State which parasite is depicted.
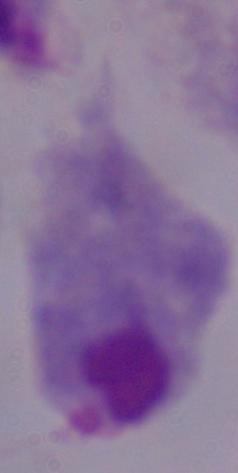
This is a trichomonad.

{
  "magnification": "1000x",
  "modality": "photomicrograph"
}